Locate every malaria parasite and every leukocyte.
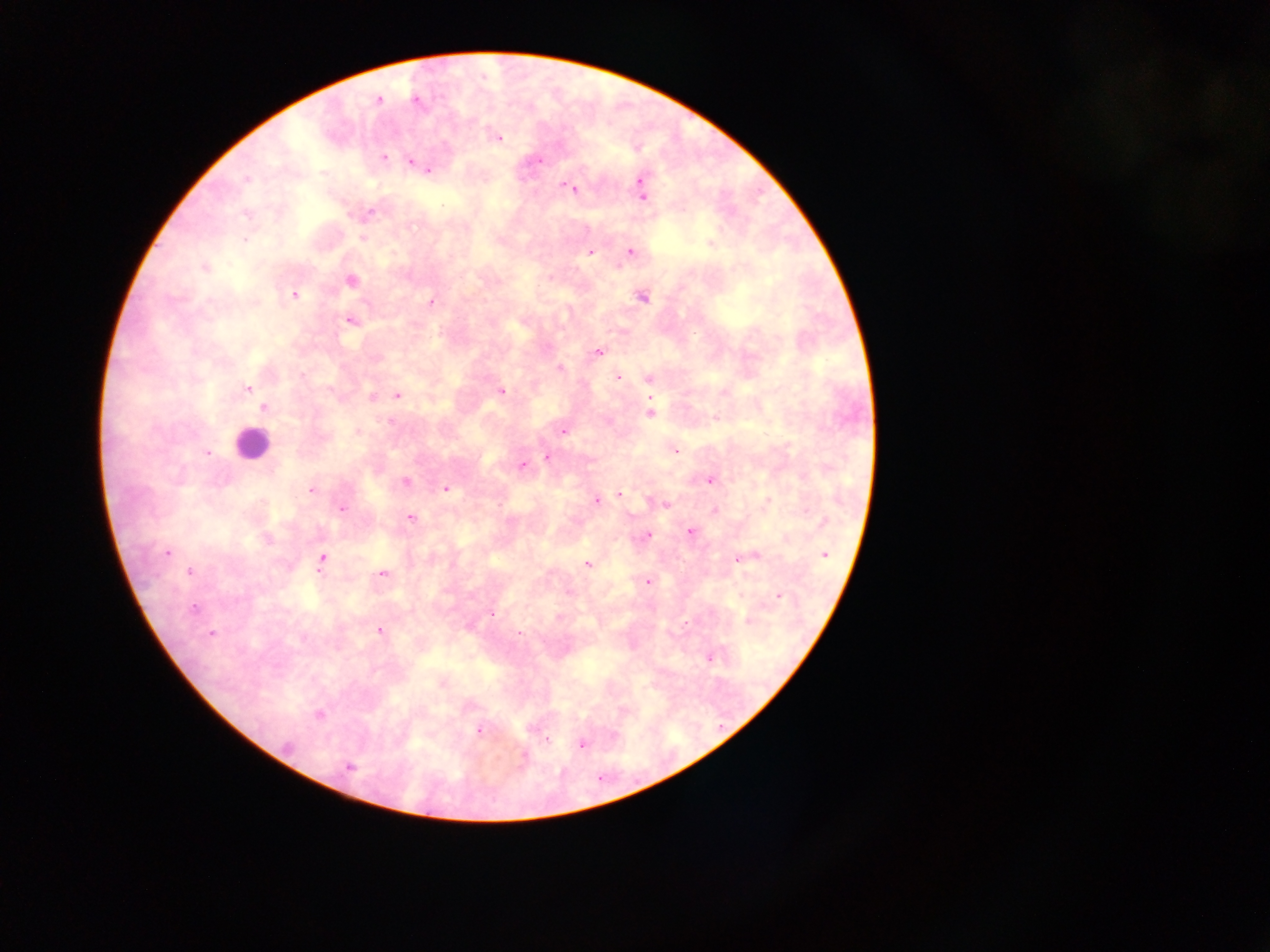

Approximate centers as {x, y} in pixels.
Malaria parasites: {378, 100}, {417, 100}, {496, 137}, {383, 157}, {538, 161}, {411, 162}, {427, 169}, {247, 178}, {640, 183}, {570, 187}, {642, 194}, {362, 238}, {710, 244}, {589, 251}, {630, 252}, {204, 267}, {350, 281}, {294, 295}, {641, 296}, {431, 302}, {350, 320}, {598, 351}, {560, 369}, {618, 376}, {649, 376}, {246, 389}, {501, 391}, {397, 395}, {371, 397}, {263, 407}, {650, 413}, {563, 431}, {358, 432}, {674, 450}, {207, 453}, {547, 457}, {522, 465}, {710, 479}, {406, 481}, {447, 488}, {311, 489}, {618, 494}, {600, 499}, {596, 500}, {662, 503}, {341, 508}, {713, 510}, {410, 518}, {690, 532}, {647, 535}, {167, 552}, {823, 554}, {738, 557}, {321, 559}, {587, 565}, {189, 572}, {381, 574}, {647, 581}, {778, 596}, {194, 608}, {491, 613}, {748, 620}, {468, 626}, {379, 631}, {211, 633}, {709, 657}, {441, 682}, {318, 715}, {479, 729}, {545, 740}, {581, 743}, {523, 757}, {349, 767}.
Leukocytes: {251, 443}.

Thick blood film. Collected in Ghana. One field of view. Mobile-phone photograph taken through the microscope. Image is 1270×952 pixels.